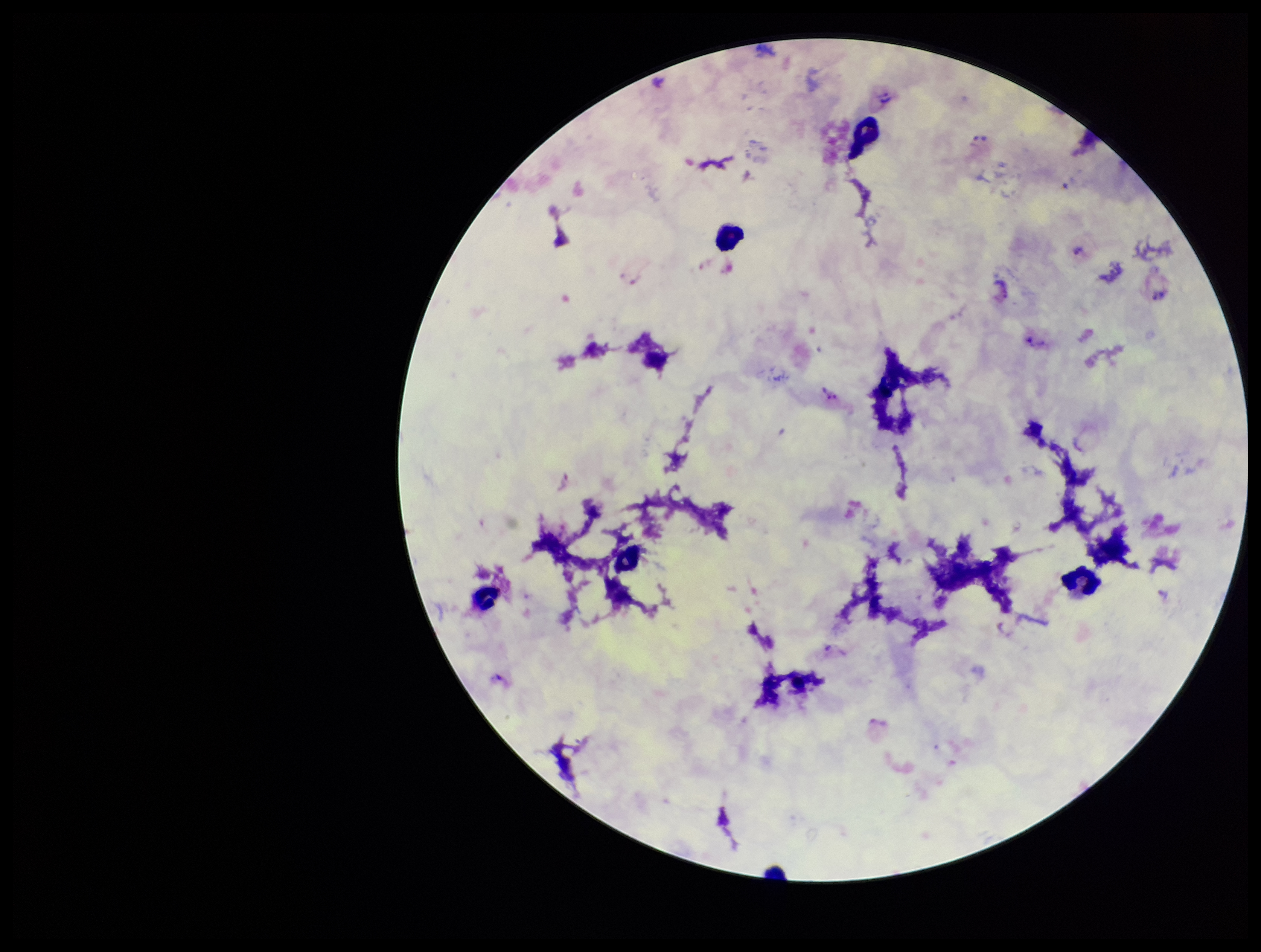

Summary:
  - Stain: Giemsa
  - Patient malaria status: positive
  - Capture: smartphone photograph through the microscope eyepiece
  - Image size: 1261×952 pixels
  - Leukocyte count: 6
  - Species reported for this patient: Plasmodium vivax
  - Parasite count: 3
  - Preparation: thick blood smear
  - Field of view: one from this slide
  - Plasmodium parasites: seen